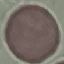 Result: negative for malaria parasites. Thin blood smear. Cell patch, automatically extracted from a larger field of view and resized to 64 × 64 pixels. Photographed with a smartphone camera at the microscope eyepiece. Giemsa stain.